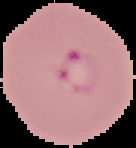

{
  "preparation": "thin blood film",
  "image_size": "136×148 pixels",
  "result": "Plasmodium parasites identified",
  "image_type": "segmented cell region with the area outside set to black"
}